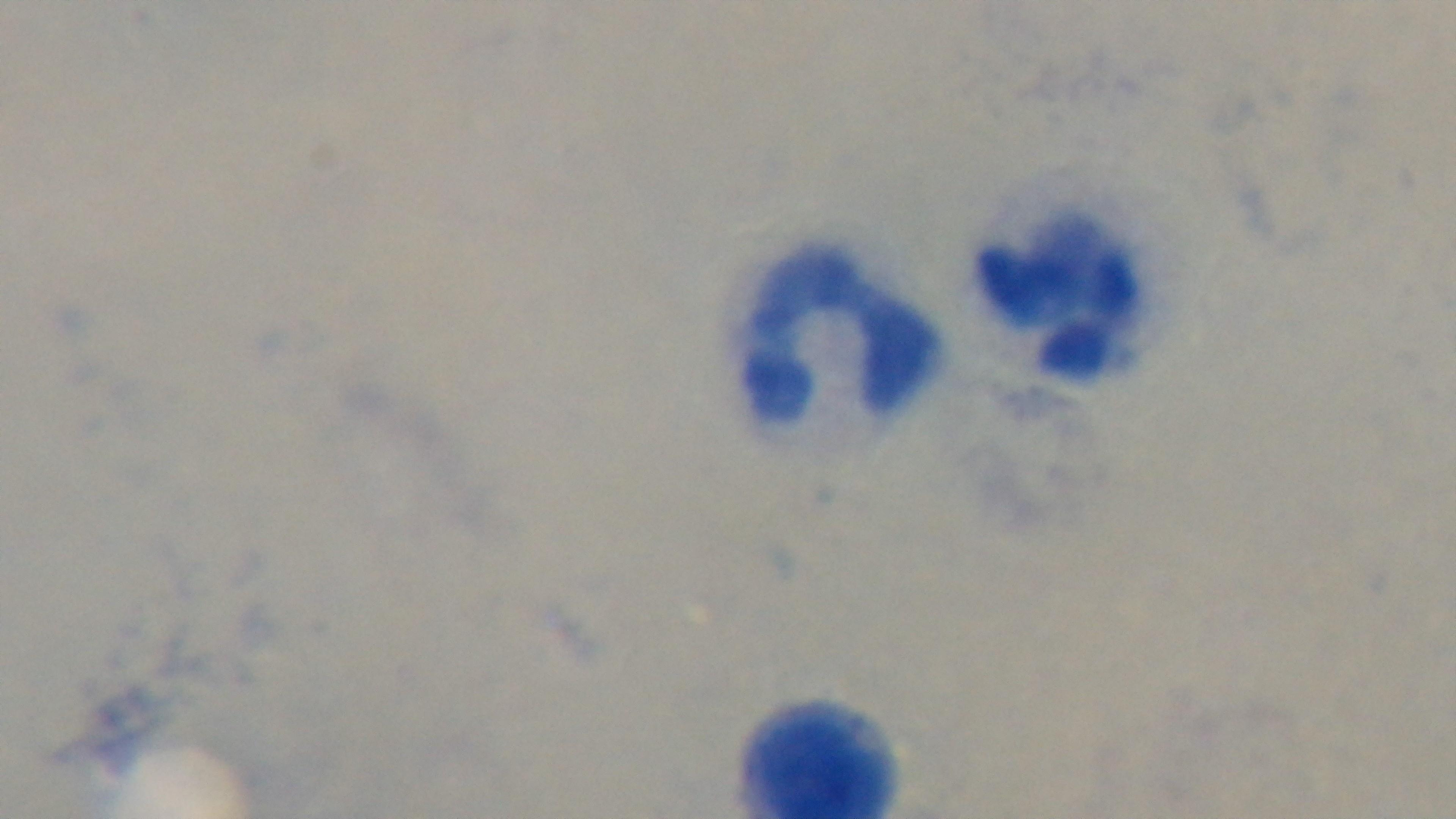 Preparation: thick. 100x oil-immersion objective. Giemsa stain. Mounted 4K digital camera. Photomicrograph. One field from the slide. Malaria status: uninfected.